Assess the morphology of the red blood cells.
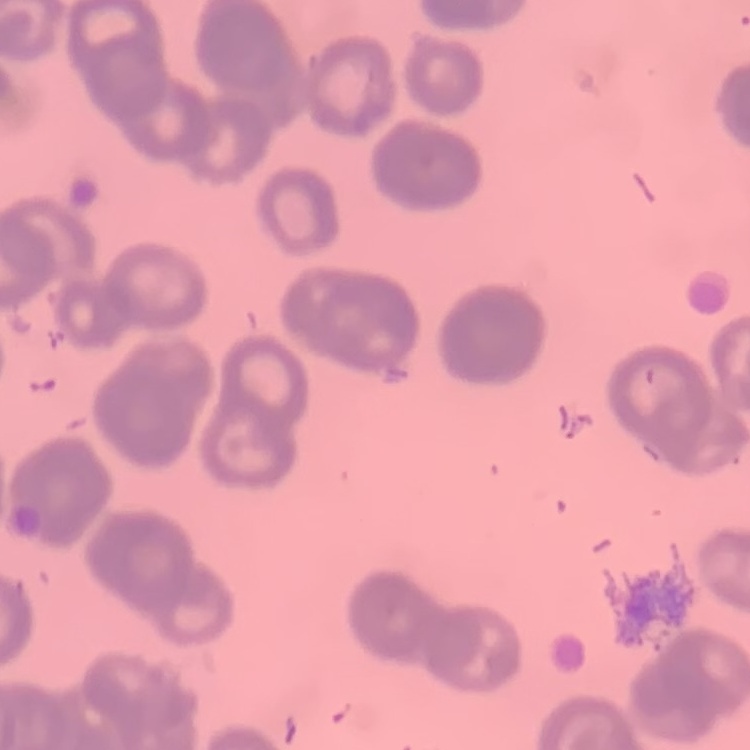

They show rouleaux formation.

One tile cut from a larger photomicrograph. Thin blood film. Stained with either Field's or Giemsa.